Classify this cell by malaria status.
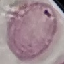
Uninfected.

Summary:
  - Stain: Giemsa
  - Capture: smartphone camera at the microscope eyepiece
  - Image type: cell patch, automatically extracted from a larger field of view and resized to 64 × 64 pixels
  - Preparation: thin blood smear